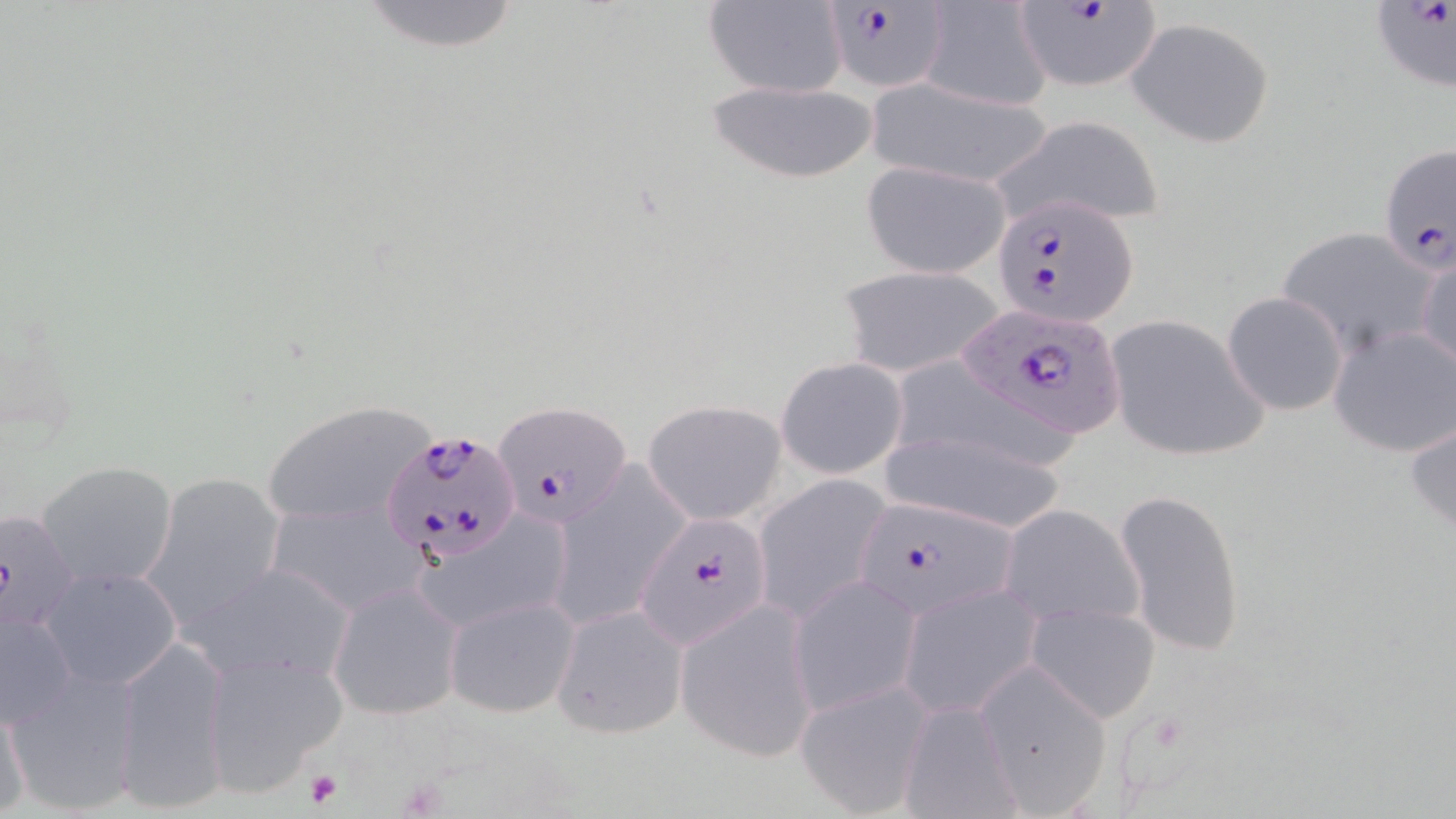
Plasmodium falciparum-infected red blood cell locations = approximate bounding boxes as [x1, y1, x2, y2] in pixels: [822, 0, 949, 95], [1008, 0, 1160, 92], [1370, 1, 1456, 91], [1379, 141, 1453, 276], [992, 191, 1141, 326], [950, 306, 1128, 444], [494, 399, 631, 530], [385, 428, 522, 564], [852, 496, 1019, 622], [637, 514, 776, 649]
slide-level diagnosis = Plasmodium falciparum
platelet locations = approximate bounding boxes as [x1, y1, x2, y2] in pixels: [305, 769, 343, 808]
modality = optical microscopy
preparation = thin blood film
stain = May-Grünwald-Giemsa
field of view = one of a larger specimen
image size = 1456×819 pixels
magnification = 1000x
uninfected red blood cell locations = approximate bounding boxes as [x1, y1, x2, y2] in pixels: [359, 0, 521, 53], [702, 0, 849, 98], [917, 3, 1051, 110], [1124, 16, 1277, 148], [701, 77, 884, 186], [866, 78, 1057, 191], [995, 114, 1166, 230], [860, 160, 1012, 278], [1277, 225, 1443, 356], [1417, 250, 1456, 377], [836, 264, 1004, 378], [1221, 292, 1347, 414], [1105, 315, 1269, 462], [1328, 322, 1456, 457], [775, 356, 909, 480], [904, 358, 1072, 468], [260, 400, 439, 530], [644, 400, 787, 525], [1406, 413, 1456, 536], [877, 422, 1072, 535], [36, 461, 178, 590], [549, 467, 692, 627], [140, 471, 286, 634], [754, 474, 893, 623], [1116, 487, 1245, 657], [265, 498, 430, 617], [996, 503, 1143, 631], [0, 507, 82, 635], [417, 512, 571, 633], [184, 564, 358, 683], [42, 566, 183, 691], [791, 575, 921, 718], [327, 580, 462, 721], [898, 585, 1041, 718], [444, 595, 579, 719], [676, 599, 820, 763], [1026, 600, 1162, 723], [549, 603, 688, 741], [0, 607, 78, 731], [114, 634, 230, 811], [200, 650, 345, 792], [974, 662, 1113, 814], [6, 669, 143, 818], [795, 681, 931, 816], [0, 694, 29, 818], [896, 700, 1021, 817]